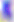

magnification: 400x
identification: Toxoplasma gondii
modality: photomicrograph